Name the cell type shown.
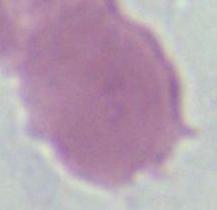

An erythrocyte.

Summary:
  - Modality: photomicrograph
  - Magnification: 1000x